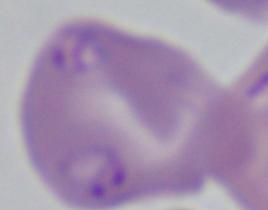 A Babesia parasite is seen. Photomicrograph. Captured at 1000x magnification.